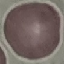
malaria status = uninfected
capture = smartphone through the microscope eyepiece
preparation = thin smear
image type = cell patch, automatically extracted from a larger field of view and resized to 64 × 64 pixels
stain = Giemsa